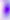
Micrograph. 400x magnification. Toxoplasma gondii is seen.